Assess the morphology of the red blood cells.
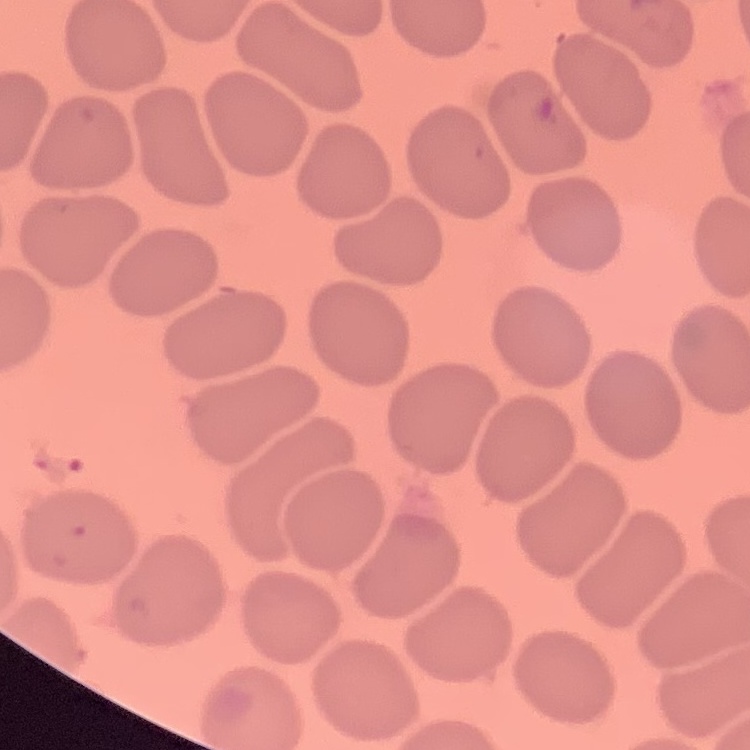
No rouleaux formation.

Summary:
  - Image type: square crop of a larger photomicrograph
  - Stain: Field's or Giemsa
  - Preparation: thin blood film